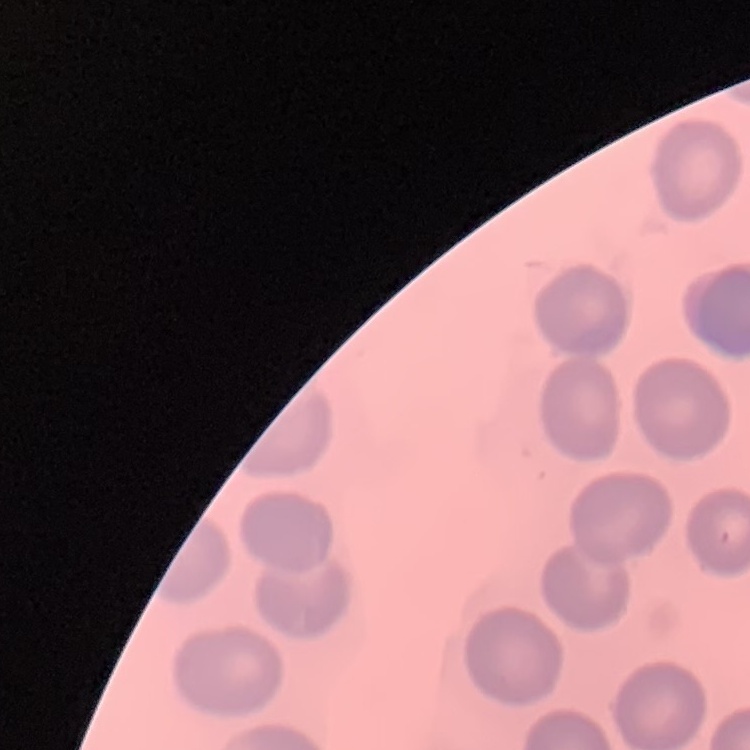
erythrocyte_morphology: no rouleaux formation
image_type: one tile cut from a larger photomicrograph
preparation: thin peripheral smear
stain: Field's or Giemsa